Give the position of every leukocyte visible.
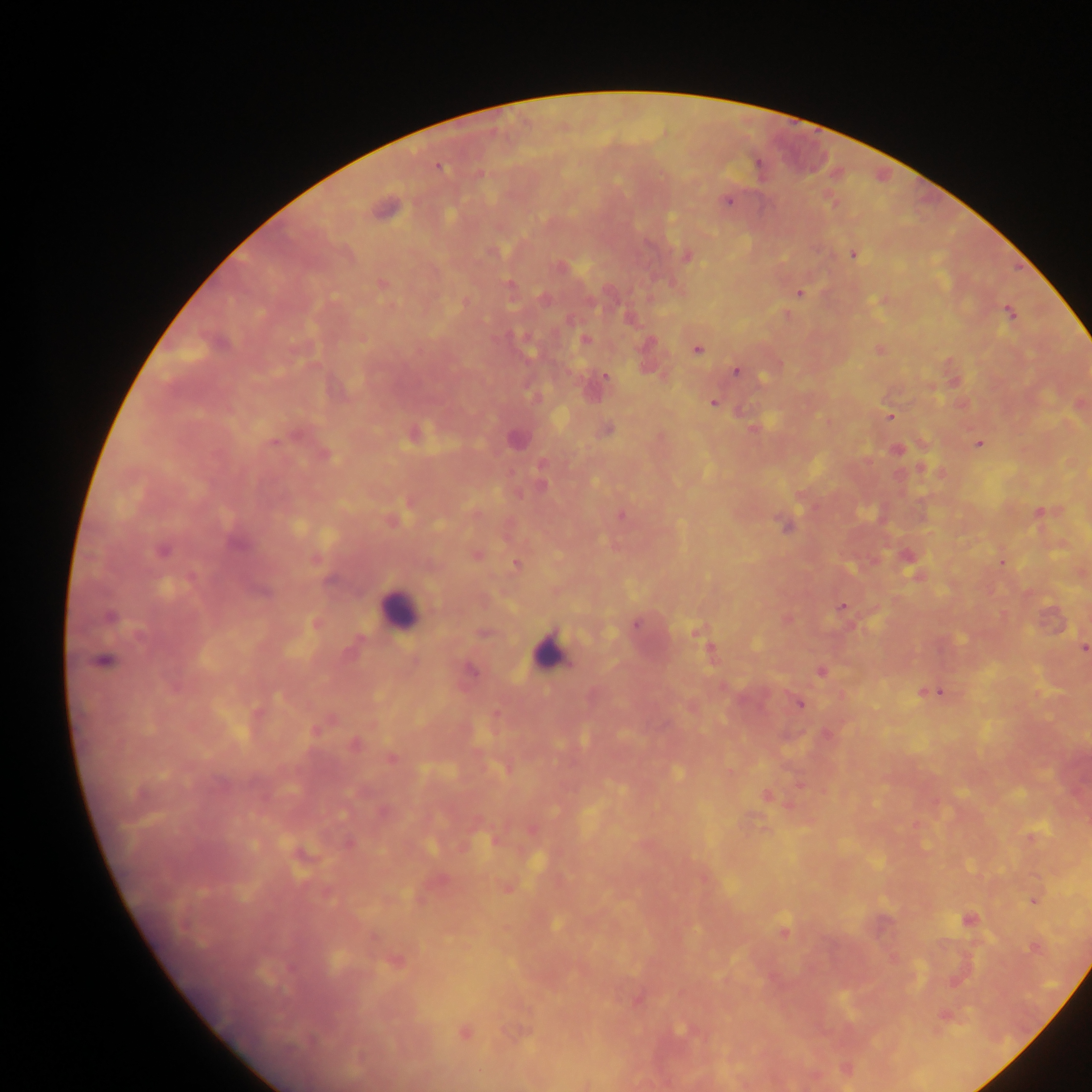
Approximate centers as (x, y) in pixels.
Leukocytes: (398, 609), (549, 651).

malaria parasite locations = approximate centers as (x, y) in pixels: (439, 166), (479, 174), (727, 201), (383, 209), (492, 252), (853, 254), (686, 257), (382, 284), (509, 286), (798, 294), (1009, 311), (585, 340), (697, 350), (880, 350), (735, 370), (605, 376), (713, 403), (890, 415), (607, 430), (517, 440), (274, 443), (979, 444), (897, 450), (542, 485), (621, 516), (785, 526), (237, 544), (162, 550), (476, 554), (1002, 563), (515, 565), (843, 607), (110, 616), (635, 625), (695, 632), (140, 637), (1084, 648), (104, 661), (471, 670), (820, 671), (933, 692), (799, 704), (315, 731), (355, 744), (391, 758), (767, 796), (1033, 900), (968, 919), (556, 923), (783, 932), (1034, 947), (398, 961), (679, 1030), (465, 1033)
preparation = thick blood smear
image size = 1092×1092 pixels
field of view = single
capture = mobile-phone photograph through a microscope
country = Ghana